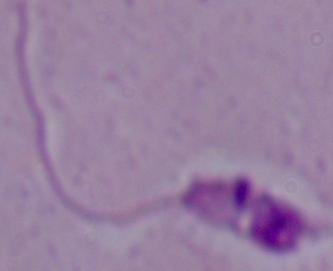
{
  "identification": "Leishmania",
  "modality": "photomicrograph",
  "magnification": "1000x"
}